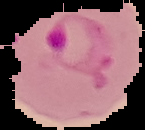
Summary:
  - Preparation: thin blood smear
  - Malaria status: parasitized
  - Image type: segmented cell region on a black background
  - Image size: 145×130 pixels